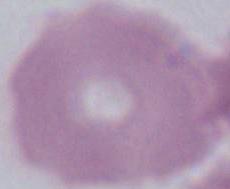
Summary:
  - Magnification: 1000x
  - Identification: erythrocyte
  - Modality: micrograph